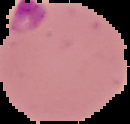
image_size: 130×124 pixels
preparation: thin blood film
image_type: cell region segmented out of the field of view; surrounding area masked to black
malaria_status: parasitized